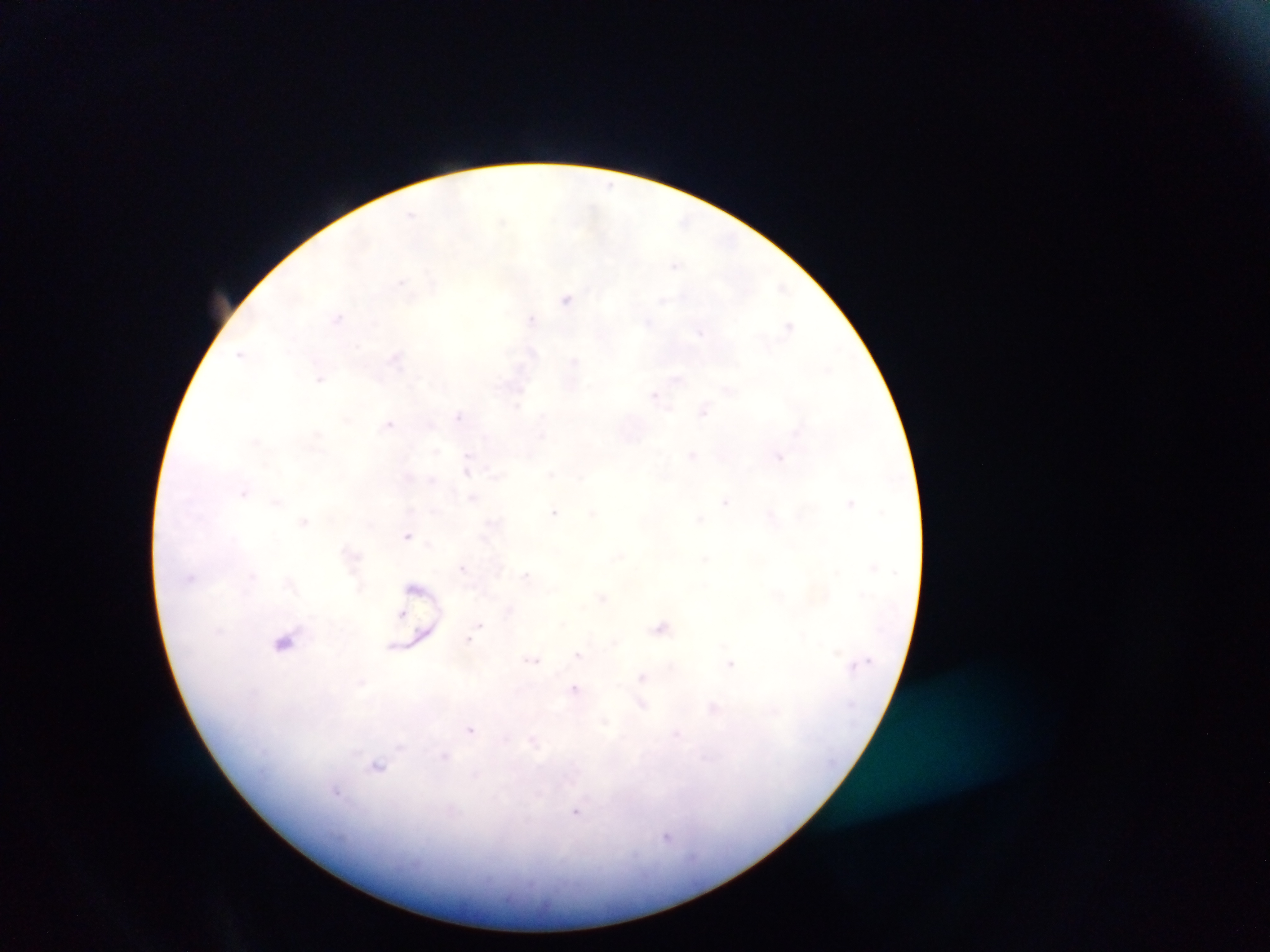
field_of_view: single
preparation: thick blood smear
image_size: 1270×952 pixels
capture: mobile-phone photograph through a microscope
plasmodium_parasite_locations: 'approximate centers as (x, y) in pixels (subset; some below the resolvable size): (400, 281), (566, 298), (338, 316), (532, 318), (789, 321), (320, 378), (655, 394), (704, 409), (458, 415), (388, 423), (779, 457), (433, 480), (473, 496), (725, 503), (554, 511), (701, 519), (407, 535), (463, 568), (526, 576), (190, 578), (510, 610), (401, 614), (480, 625), (661, 626), (468, 638), (578, 654), (533, 659), (729, 666), (575, 688), (471, 730), (337, 792), (576, 814), (667, 837)'
country: Ghana